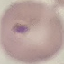
Summary:
  - Malaria status: parasitized
  - Stain: Giemsa
  - Image type: automatically extracted cell patch, resized to 64 × 64 pixels
  - Capture: smartphone camera at the microscope eyepiece
  - Preparation: thin blood film